Outline each blood parasite and name the species.
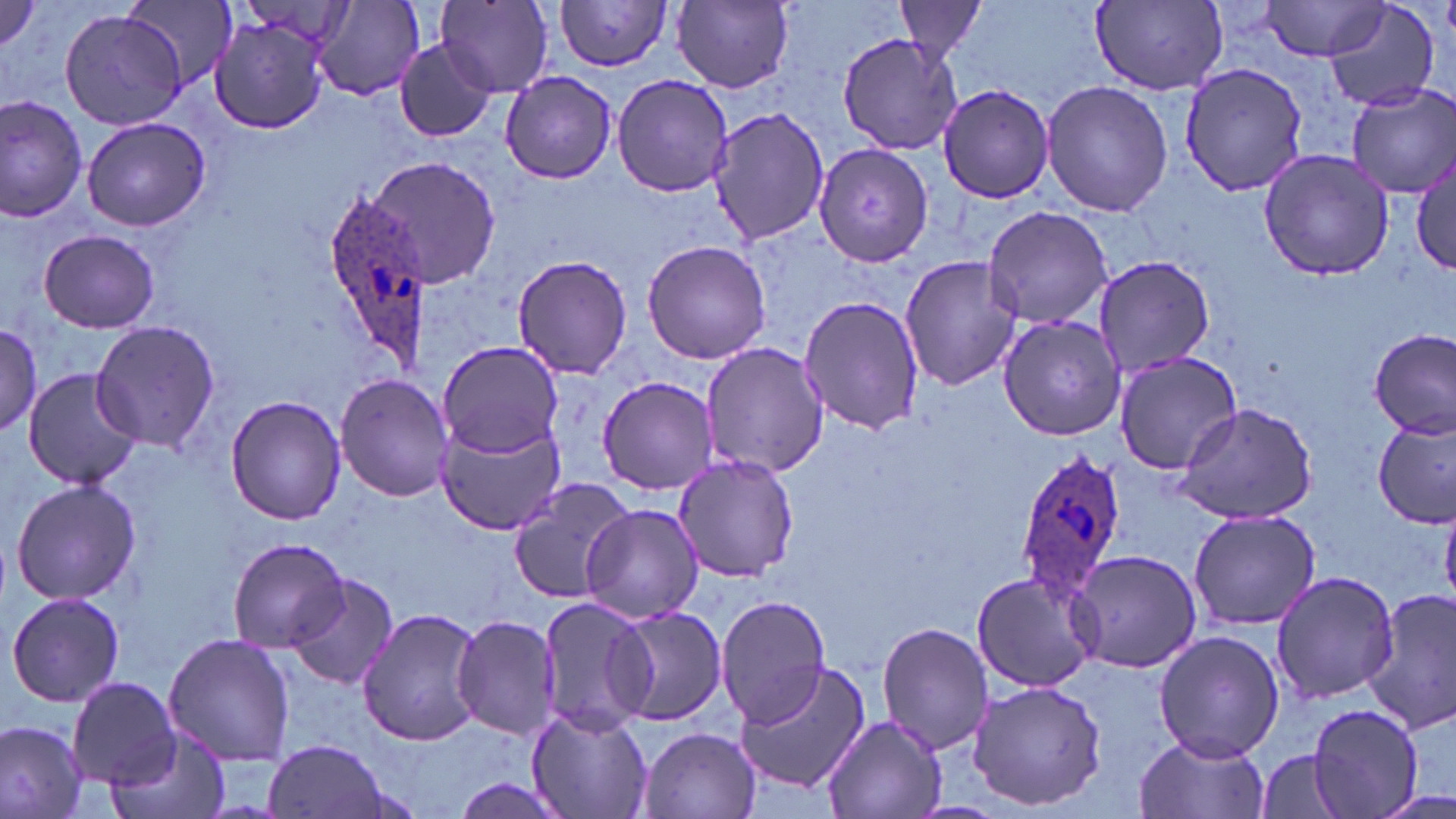

Approximate bounding boxes as named x1/y1/x2/y2 corners in pixels.
Plasmodium ovale-infected red blood cells: (x1=322, y1=193, x2=433, y2=360), (x1=1014, y1=447, x2=1127, y2=596).
No Plasmodium falciparum, Plasmodium malariae, Plasmodium vivax, Babesia divergens, or Trypanosoma brucei observed.

{
  "slide_level_diagnosis": "Plasmodium ovale",
  "field_of_view": "one of a larger specimen",
  "image_size": "1456×819 pixels",
  "stain": "May-Grünwald-Giemsa",
  "magnification": "1000x",
  "preparation": "thin blood smear",
  "modality": "light microscopy",
  "uninfected_red_blood_cell_locations": "approximate bounding boxes as named x1/y1/x2/y2 corners in pixels: (x1=0, y1=0, x2=46, y2=55), (x1=120, y1=0, x2=235, y2=98), (x1=311, y1=0, x2=427, y2=102), (x1=554, y1=0, x2=675, y2=72), (x1=1089, y1=0, x2=1229, y2=94), (x1=1322, y1=0, x2=1442, y2=112), (x1=437, y1=1, x2=555, y2=96), (x1=672, y1=1, x2=794, y2=90), (x1=894, y1=1, x2=990, y2=61), (x1=1259, y1=1, x2=1389, y2=61), (x1=59, y1=9, x2=189, y2=130), (x1=209, y1=14, x2=331, y2=134), (x1=837, y1=31, x2=962, y2=157), (x1=392, y1=38, x2=498, y2=142), (x1=1177, y1=62, x2=1309, y2=196), (x1=501, y1=72, x2=618, y2=184), (x1=611, y1=72, x2=733, y2=198), (x1=1041, y1=80, x2=1174, y2=217), (x1=936, y1=83, x2=1055, y2=204), (x1=1347, y1=85, x2=1455, y2=197), (x1=0, y1=97, x2=87, y2=224), (x1=707, y1=108, x2=831, y2=247), (x1=80, y1=116, x2=209, y2=231), (x1=813, y1=145, x2=936, y2=267), (x1=1258, y1=148, x2=1395, y2=281), (x1=1413, y1=151, x2=1455, y2=274), (x1=363, y1=156, x2=501, y2=288), (x1=982, y1=205, x2=1113, y2=329), (x1=38, y1=229, x2=160, y2=333), (x1=642, y1=238, x2=771, y2=364), (x1=511, y1=253, x2=632, y2=380), (x1=899, y1=253, x2=1024, y2=393), (x1=1092, y1=254, x2=1214, y2=377), (x1=798, y1=293, x2=922, y2=434), (x1=998, y1=313, x2=1129, y2=441), (x1=0, y1=319, x2=45, y2=435), (x1=91, y1=320, x2=225, y2=453), (x1=1369, y1=329, x2=1455, y2=439), (x1=437, y1=338, x2=563, y2=458), (x1=702, y1=343, x2=825, y2=477), (x1=1112, y1=350, x2=1244, y2=474), (x1=23, y1=368, x2=146, y2=490), (x1=333, y1=372, x2=453, y2=501), (x1=597, y1=376, x2=723, y2=495), (x1=225, y1=393, x2=345, y2=525), (x1=1173, y1=401, x2=1322, y2=527), (x1=1374, y1=418, x2=1455, y2=529), (x1=433, y1=420, x2=564, y2=535), (x1=670, y1=453, x2=802, y2=583), (x1=507, y1=476, x2=634, y2=604), (x1=9, y1=477, x2=143, y2=606), (x1=579, y1=503, x2=704, y2=622), (x1=1189, y1=508, x2=1320, y2=631), (x1=226, y1=536, x2=351, y2=651), (x1=1066, y1=549, x2=1204, y2=675), (x1=970, y1=569, x2=1099, y2=693), (x1=1270, y1=570, x2=1399, y2=704), (x1=284, y1=571, x2=399, y2=690), (x1=1362, y1=587, x2=1456, y2=733), (x1=6, y1=591, x2=124, y2=707), (x1=716, y1=595, x2=832, y2=725), (x1=535, y1=596, x2=657, y2=734), (x1=612, y1=605, x2=728, y2=726), (x1=357, y1=606, x2=485, y2=747), (x1=451, y1=613, x2=561, y2=741), (x1=878, y1=621, x2=993, y2=756), (x1=1153, y1=629, x2=1284, y2=763), (x1=162, y1=632, x2=297, y2=766), (x1=732, y1=659, x2=871, y2=795), (x1=68, y1=676, x2=181, y2=787), (x1=969, y1=678, x2=1106, y2=810), (x1=1304, y1=702, x2=1426, y2=818), (x1=524, y1=705, x2=653, y2=819), (x1=822, y1=715, x2=946, y2=819), (x1=0, y1=720, x2=87, y2=818), (x1=638, y1=725, x2=763, y2=819), (x1=108, y1=730, x2=229, y2=819), (x1=1134, y1=734, x2=1267, y2=819), (x1=261, y1=738, x2=396, y2=818), (x1=1255, y1=750, x2=1353, y2=818), (x1=447, y1=777, x2=577, y2=819)"
}